Name the cell type shown.
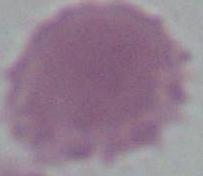

This is an erythrocyte.

Summary:
  - Modality: photomicrograph
  - Magnification: 1000x